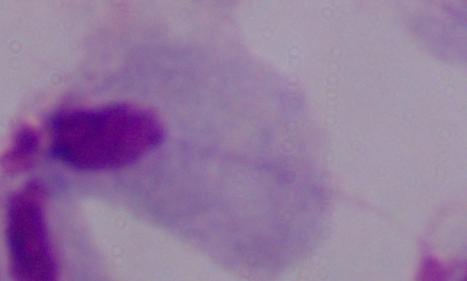
Summary:
  - Modality: photomicrograph
  - Magnification: 1000x
  - Identification: trichomonad